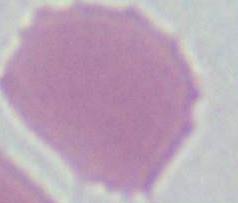

{
  "modality": "photomicrograph",
  "magnification": "1000x",
  "identification": "red blood cell"
}